Outline each uninfected red blood cell.
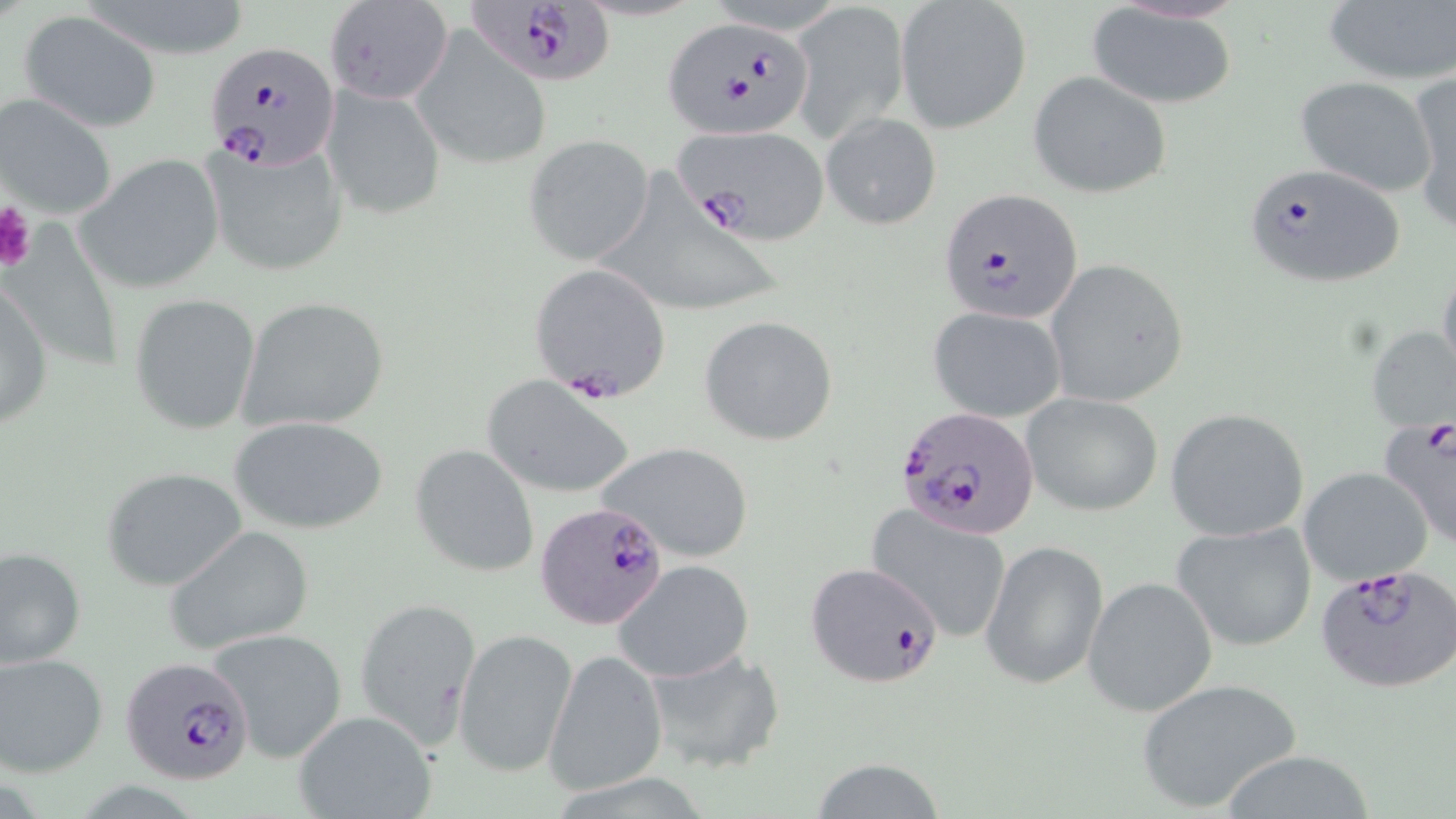
Approximate bounding boxes as named x1/y1/x2/y2 corners in pixels.
Uninfected red blood cells (subset): (x1=896, y1=0, x2=1032, y2=133), (x1=1321, y1=0, x2=1456, y2=88), (x1=792, y1=2, x2=910, y2=141), (x1=1086, y1=4, x2=1238, y2=109), (x1=19, y1=11, x2=161, y2=132), (x1=410, y1=25, x2=553, y2=171), (x1=1028, y1=72, x2=1172, y2=200), (x1=1408, y1=72, x2=1456, y2=234), (x1=1293, y1=74, x2=1434, y2=197), (x1=322, y1=81, x2=447, y2=220), (x1=1, y1=92, x2=118, y2=221), (x1=820, y1=112, x2=941, y2=231), (x1=524, y1=135, x2=653, y2=265), (x1=204, y1=140, x2=349, y2=276), (x1=76, y1=153, x2=226, y2=293), (x1=605, y1=163, x2=780, y2=318), (x1=1046, y1=258, x2=1190, y2=408), (x1=1437, y1=263, x2=1456, y2=385), (x1=0, y1=275, x2=52, y2=431), (x1=129, y1=291, x2=262, y2=434), (x1=238, y1=296, x2=391, y2=433), (x1=929, y1=307, x2=1067, y2=422), (x1=699, y1=315, x2=839, y2=447), (x1=1367, y1=324, x2=1456, y2=434), (x1=482, y1=379, x2=635, y2=497), (x1=1022, y1=392, x2=1164, y2=516), (x1=1165, y1=408, x2=1313, y2=543), (x1=230, y1=415, x2=391, y2=535), (x1=595, y1=440, x2=755, y2=562), (x1=410, y1=443, x2=540, y2=577), (x1=1299, y1=466, x2=1434, y2=585), (x1=101, y1=467, x2=247, y2=590), (x1=866, y1=503, x2=1015, y2=644), (x1=1171, y1=520, x2=1319, y2=653), (x1=163, y1=525, x2=316, y2=654), (x1=981, y1=539, x2=1109, y2=691), (x1=0, y1=544, x2=86, y2=669), (x1=612, y1=559, x2=755, y2=683), (x1=1083, y1=576, x2=1218, y2=716), (x1=354, y1=597, x2=483, y2=747), (x1=205, y1=626, x2=348, y2=763), (x1=452, y1=627, x2=579, y2=778), (x1=639, y1=643, x2=785, y2=773), (x1=545, y1=648, x2=668, y2=797), (x1=0, y1=652, x2=109, y2=777), (x1=1135, y1=679, x2=1302, y2=812), (x1=289, y1=708, x2=440, y2=819), (x1=1219, y1=749, x2=1377, y2=818), (x1=805, y1=758, x2=952, y2=818).

slide-level diagnosis = Plasmodium falciparum
stain = May-Grünwald-Giemsa
magnification = 1000x
Plasmodium falciparum-infected red blood cell locations (subset) = approximate bounding boxes as named x1/y1/x2/y2 corners in pixels: (x1=463, y1=0, x2=617, y2=89), (x1=664, y1=18, x2=813, y2=139), (x1=207, y1=37, x2=338, y2=170), (x1=670, y1=123, x2=831, y2=244), (x1=1239, y1=162, x2=1407, y2=290), (x1=937, y1=188, x2=1084, y2=324), (x1=528, y1=262, x2=672, y2=403), (x1=895, y1=406, x2=1043, y2=540), (x1=1378, y1=415, x2=1456, y2=548), (x1=537, y1=500, x2=669, y2=631), (x1=803, y1=560, x2=945, y2=689), (x1=1315, y1=564, x2=1456, y2=694), (x1=121, y1=655, x2=257, y2=785)
preparation = thin blood film
modality = optical microscopy
image size = 1456×819 pixels
field of view = single
platelet locations = approximate bounding boxes as named x1/y1/x2/y2 corners in pixels: (x1=0, y1=201, x2=37, y2=273)